Comment on the morphology of the red blood cells.
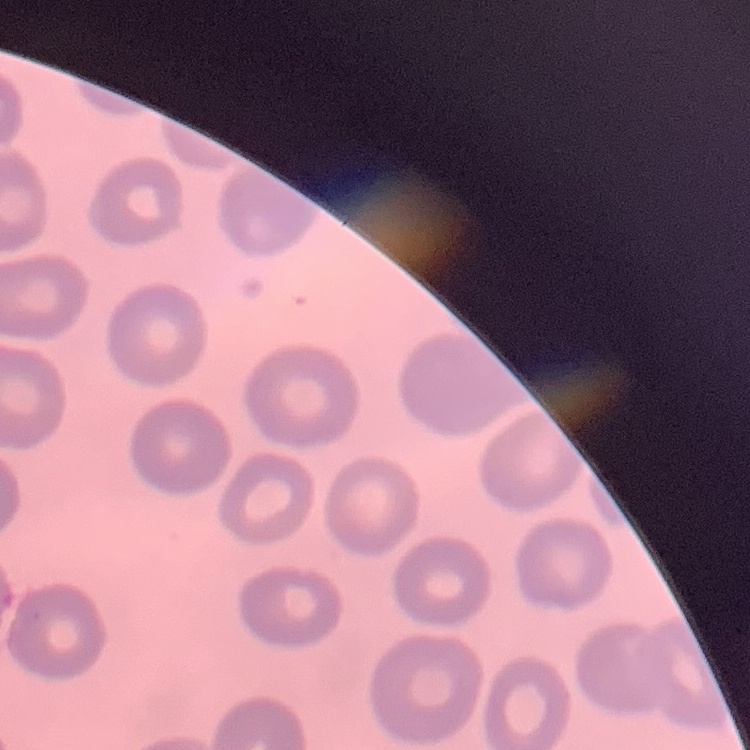

No rouleaux formation.

Thin peripheral smear. Stained with either Field's or Giemsa. One tile cut from a larger photomicrograph.